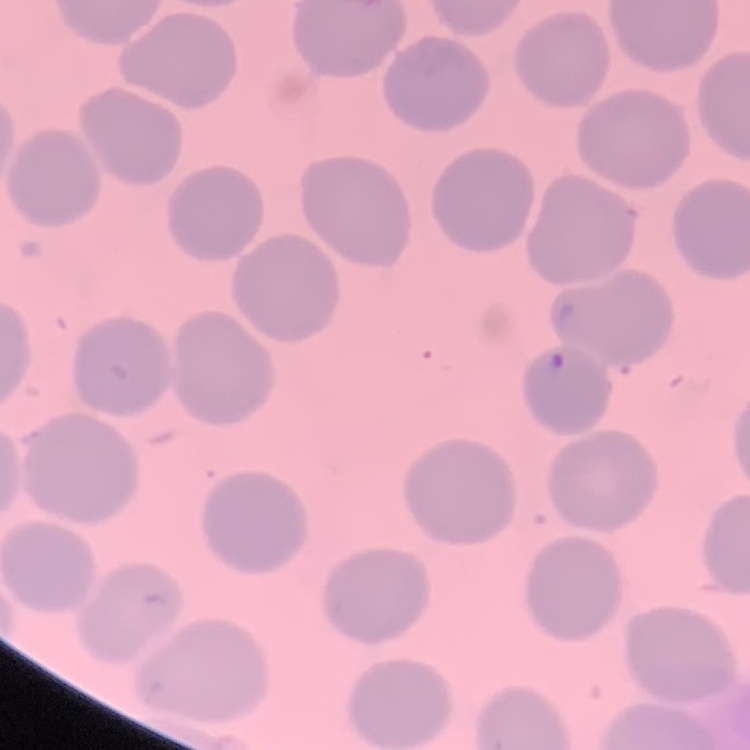
Summary:
  - Red blood cell morphology: no rouleaux formation
  - Preparation: thin blood film
  - Stain: Field's or Giemsa
  - Image type: square crop of a larger photomicrograph